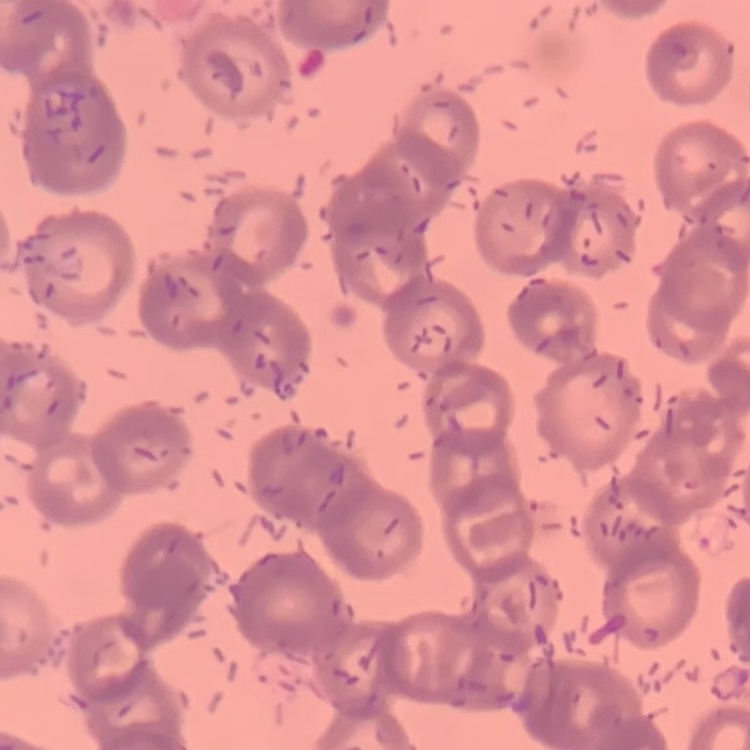
{
  "erythrocyte_morphology": "rouleaux formation",
  "stain": "Field's or Giemsa",
  "preparation": "thin blood film",
  "image_type": "square crop of a larger photomicrograph"
}